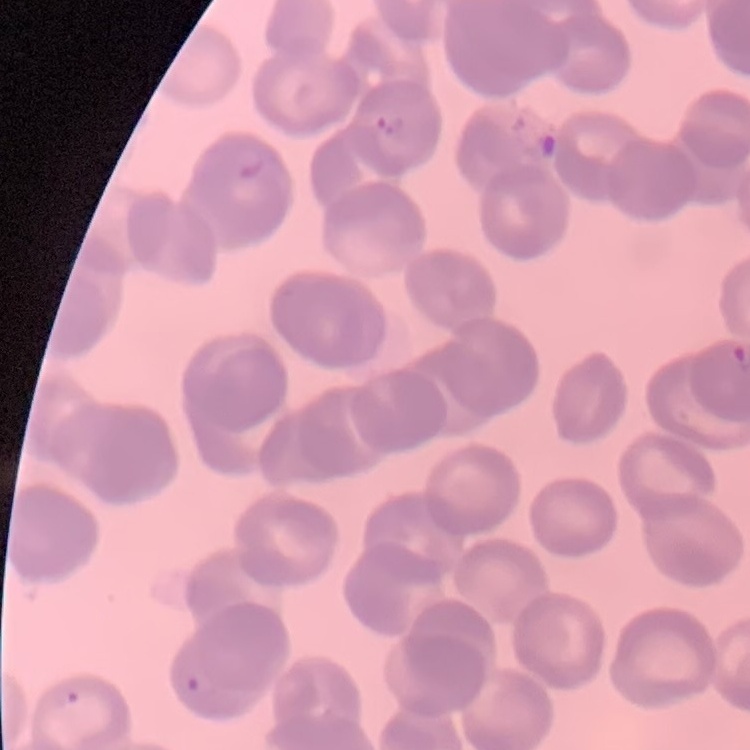
red blood cell morphology = rouleaux formation
image type = one tile cut from a larger photomicrograph
stain = Field's or Giemsa
preparation = thin peripheral smear